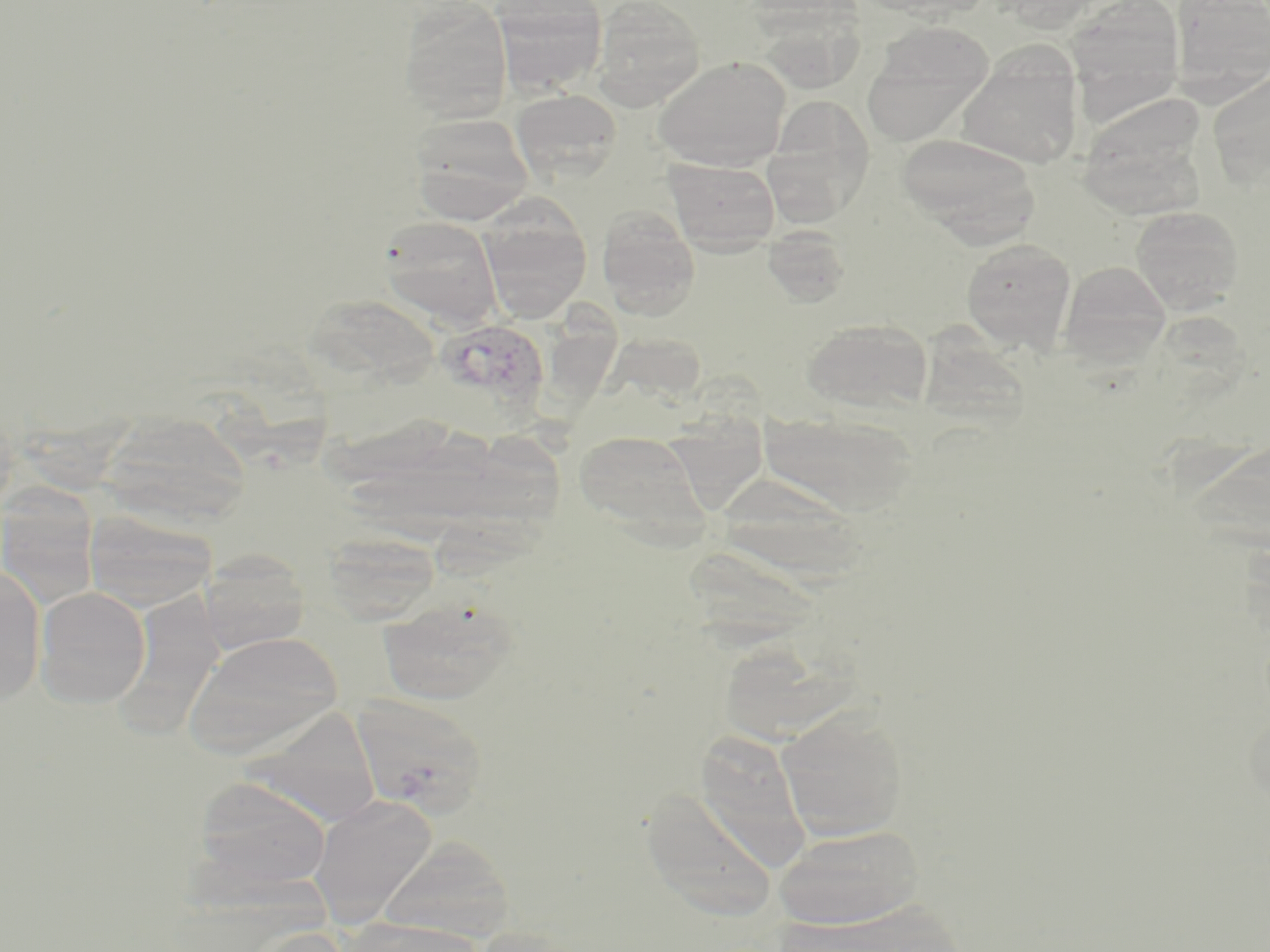

Approximate bounding boxes as (x1, y1, x2, y2) in pixels. Uninfected red blood cell locations: (492, 0, 608, 95), (591, 0, 706, 110), (1061, 0, 1187, 115), (1169, 1, 1270, 98), (398, 2, 513, 123), (863, 24, 994, 146), (956, 52, 1084, 170), (653, 56, 791, 172), (1206, 69, 1270, 189), (510, 88, 623, 183), (763, 96, 876, 223), (409, 112, 534, 222), (896, 133, 1040, 244), (663, 157, 781, 254), (477, 203, 592, 325), (1129, 206, 1245, 315), (596, 207, 701, 317), (378, 216, 501, 327), (762, 226, 852, 308), (960, 237, 1077, 353), (1059, 260, 1171, 366), (302, 293, 439, 392), (800, 317, 934, 414), (760, 408, 918, 516), (100, 411, 252, 529), (572, 428, 710, 542), (709, 472, 870, 584), (0, 483, 100, 609), (84, 510, 216, 611), (321, 532, 439, 624), (199, 551, 309, 656), (0, 564, 46, 707), (34, 586, 150, 708), (378, 597, 518, 706), (185, 631, 343, 756), (352, 693, 490, 817), (245, 706, 383, 827), (776, 708, 909, 841), (693, 729, 812, 868), (191, 777, 333, 893), (638, 785, 779, 923), (309, 794, 438, 927), (773, 823, 926, 929), (378, 835, 516, 942), (345, 917, 483, 952), (243, 925, 355, 952). Plasmodium vivax-infected red blood cell locations: (432, 318, 550, 423). Slide-level diagnosis: Plasmodium vivax. Image is 1270×952 pixels. May-Grünwald-Giemsa-stained preparation. Thin blood film. One field of a larger specimen. Captured at 1000x magnification. Optical microscopy.